Point out each malaria parasite and each leukocyte.
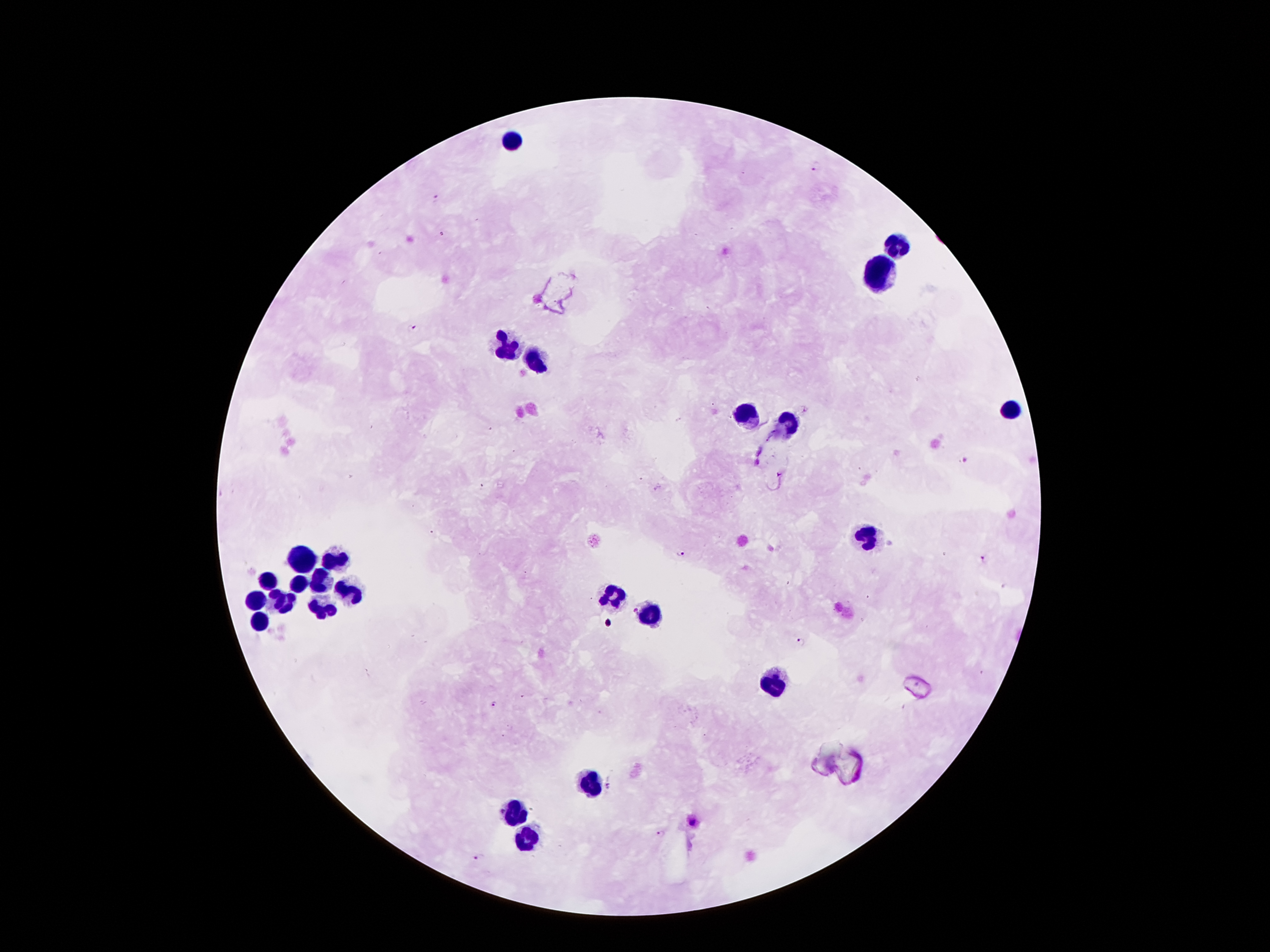
Approximate centers as (x, y) in pixels.
Malaria parasites: (817, 166), (438, 199), (411, 330), (965, 460), (481, 485), (679, 553), (983, 558), (801, 643), (523, 697), (493, 704), (609, 786), (693, 822), (661, 833), (478, 857).
Leukocytes: (510, 142), (892, 244), (875, 276), (505, 348), (533, 358), (1011, 411), (745, 413), (787, 423), (864, 537), (300, 557), (335, 557), (319, 581), (270, 582), (297, 583), (274, 592), (348, 593), (608, 595), (254, 600), (286, 604), (323, 610), (648, 614), (259, 619), (768, 684), (590, 782), (516, 810), (530, 837).

capture = smartphone camera through the microscope eyepiece
field of view = one from this slide
patient malaria status = infected with Plasmodium falciparum
preparation = thick blood smear
stain = Giemsa
image size = 1270×952 pixels
magnification = 100x